State which parasite is depicted.
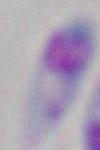

Toxoplasma gondii.

Summary:
  - Magnification: 1000x
  - Modality: micrograph